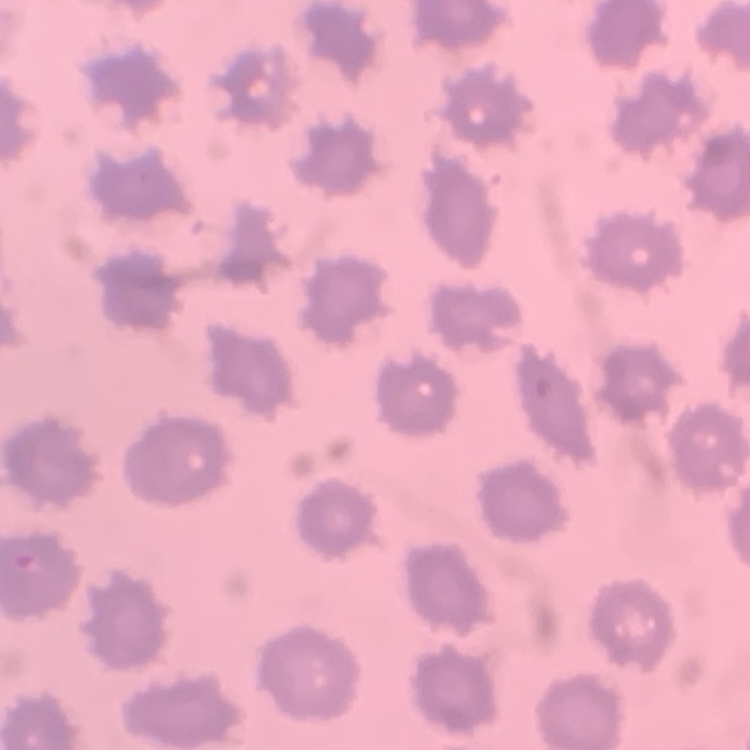

Summary:
  - Red blood cell morphology: no rouleaux formation
  - Stain: Field's or Giemsa
  - Image type: square crop of a larger photomicrograph
  - Preparation: thin blood smear